Comment on the morphology of the erythrocytes.
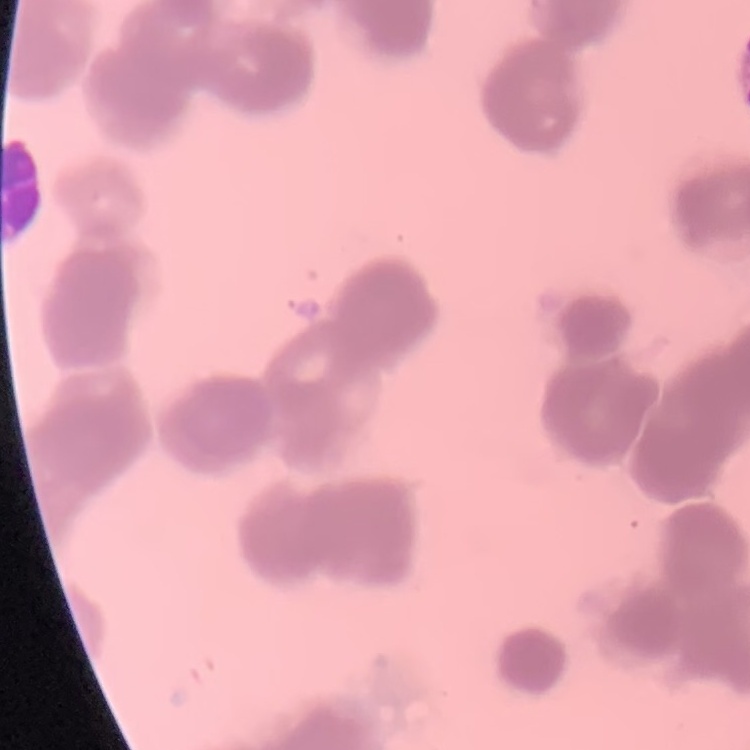
They show rouleaux formation.

Stained with either Field's or Giemsa. Thin peripheral smear. One tile cut from a larger photomicrograph.